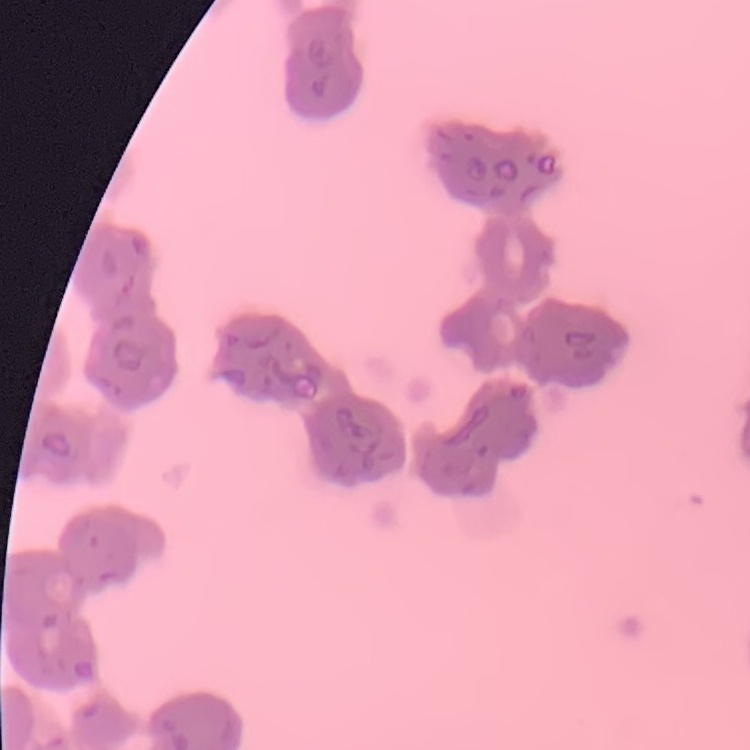

{
  "erythrocyte_morphology": "rouleaux formation",
  "image_type": "one tile cut from a larger photomicrograph",
  "stain": "Field's or Giemsa",
  "preparation": "thin blood film"
}